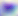

Summary:
  - Modality: photomicrograph
  - Identification: Toxoplasma gondii
  - Magnification: 400x